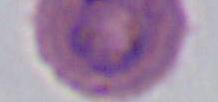

modality = photomicrograph
magnification = 400x or 1000x
identification = Plasmodium